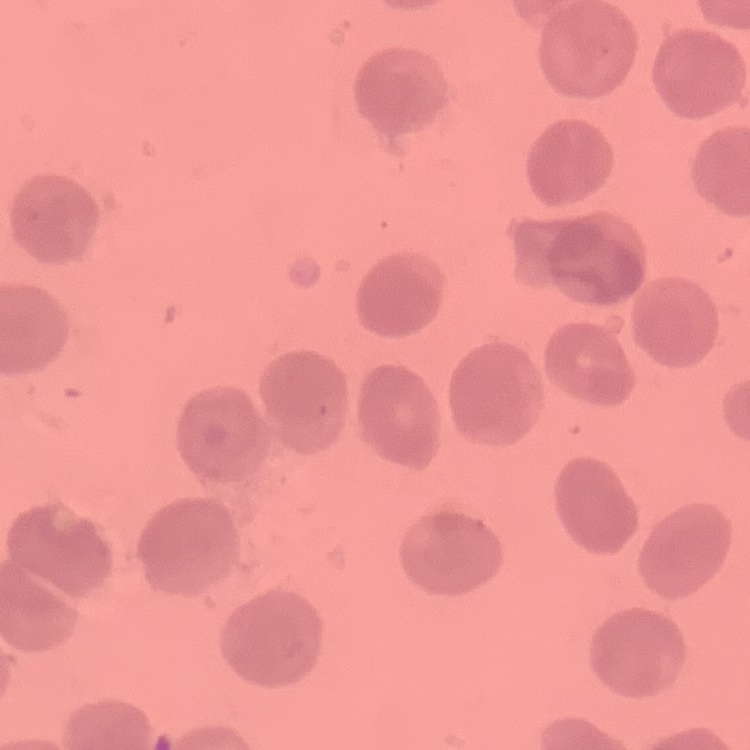
The erythrocytes exhibit no rouleaux formation. Stained with either Field's or Giemsa. Square crop of a larger photomicrograph. Thin peripheral smear.